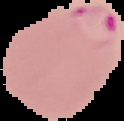
Summary:
  - Image type: segmented cell region on a black background
  - Malaria status: parasitized
  - Image size: 124×121 pixels
  - Preparation: thin blood smear